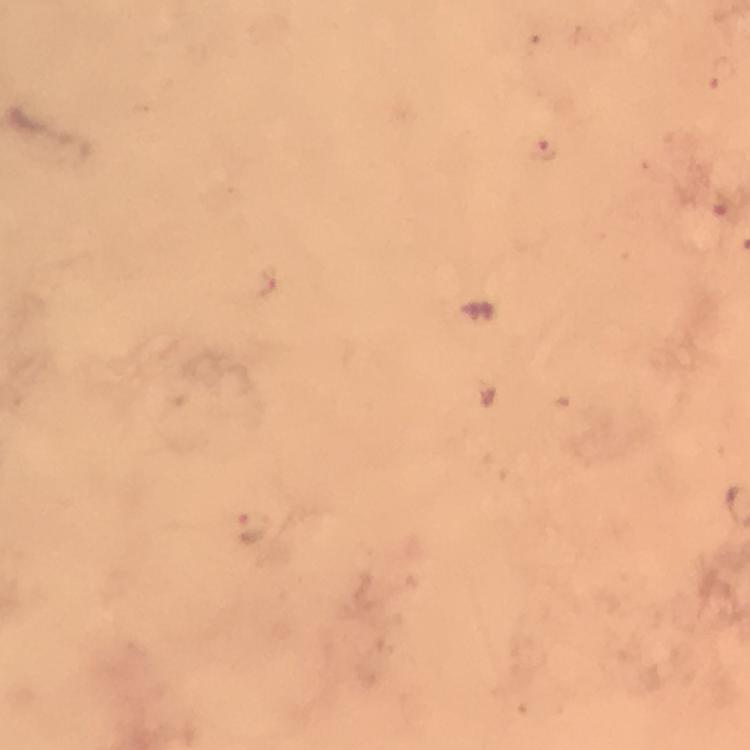
{
  "stain": "Giemsa",
  "plasmodium_parasite_locations": "approximate object centers, in pixels from the top-left corner: (x=720, y=73), (x=544, y=149), (x=256, y=528)",
  "capture": "smartphone mounted on the microscope",
  "preparation": "thick blood film",
  "image_size": "750×750 pixels",
  "context": "from a malaria diagnostic workup",
  "cropped_from": "a single field of view",
  "immersion_oil": "applied",
  "magnification": "100x"
}